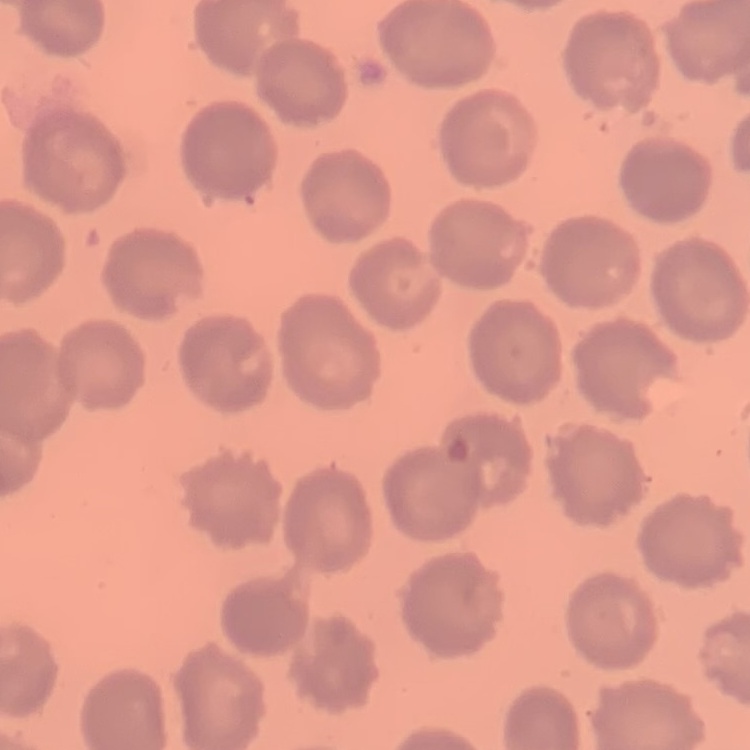

Summary:
  - Erythrocyte morphology: no rouleaux formation
  - Stain: Field's or Giemsa
  - Preparation: thin blood smear
  - Image type: one tile cut from a larger photomicrograph